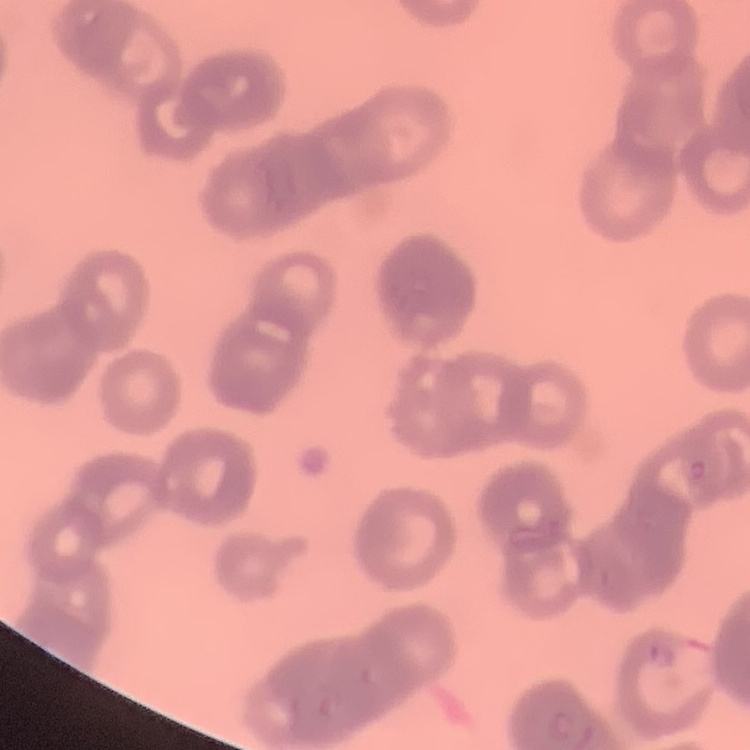 The red blood cells exhibit rouleaux formation. Thin peripheral smear. Field's or Giemsa stain. One tile cut from a larger photomicrograph.